Comment on the morphology of the erythrocytes.
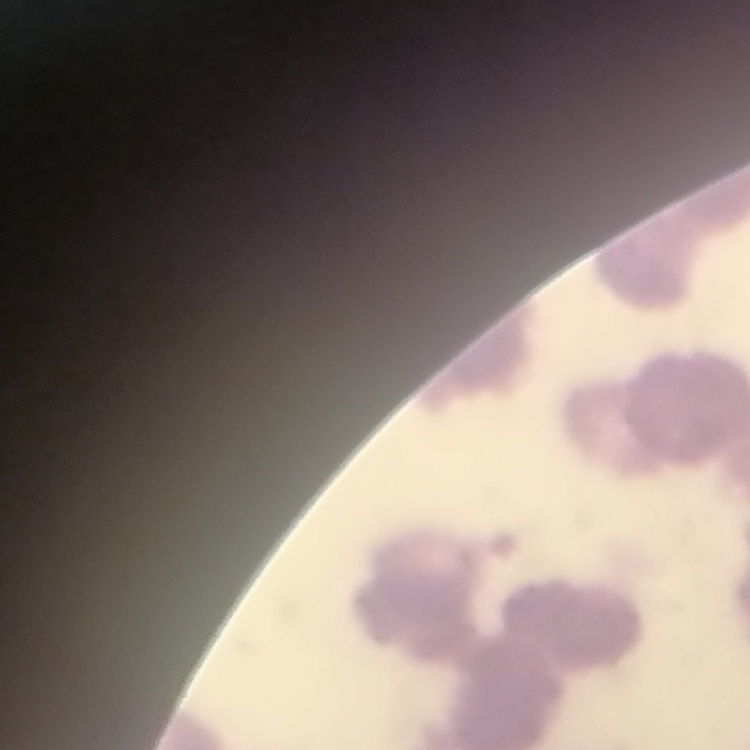
Rouleaux formation.

Thin blood smear. Field's or Giemsa stain. One tile cut from a larger photomicrograph.